Report the malaria status of this cell.
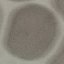

It is uninfected.

{
  "capture": "smartphone through the microscope eyepiece",
  "image_type": "cell patch, automatically extracted from a larger field of view and resized to 64 × 64 pixels",
  "preparation": "thin blood smear",
  "stain": "Giemsa"
}